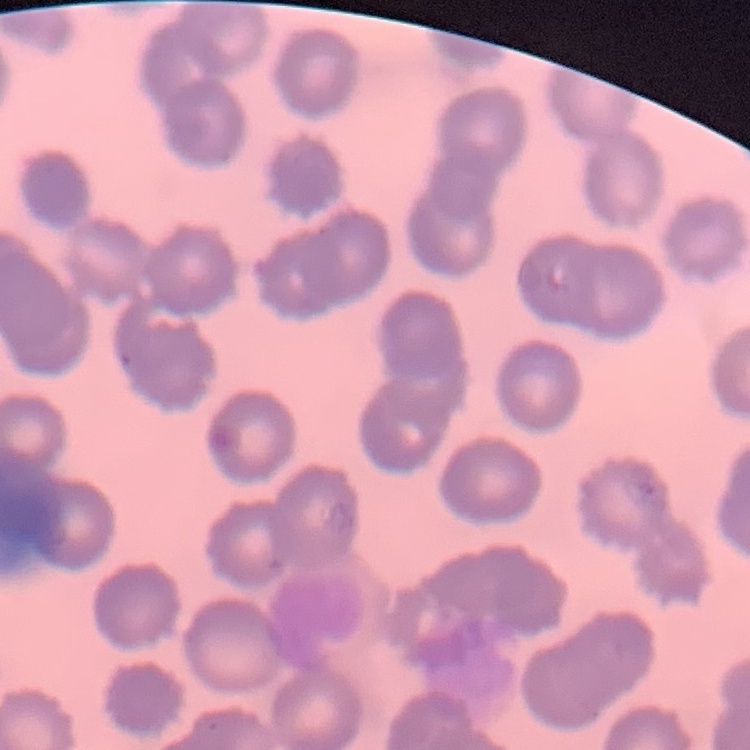

Summary:
  - Red blood cell morphology: no rouleaux formation
  - Stain: Field's or Giemsa
  - Image type: square crop of a larger photomicrograph
  - Preparation: thin blood smear